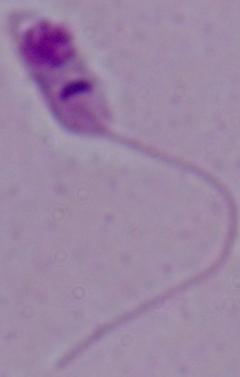

identification = Leishmania
magnification = 1000x
modality = photomicrograph